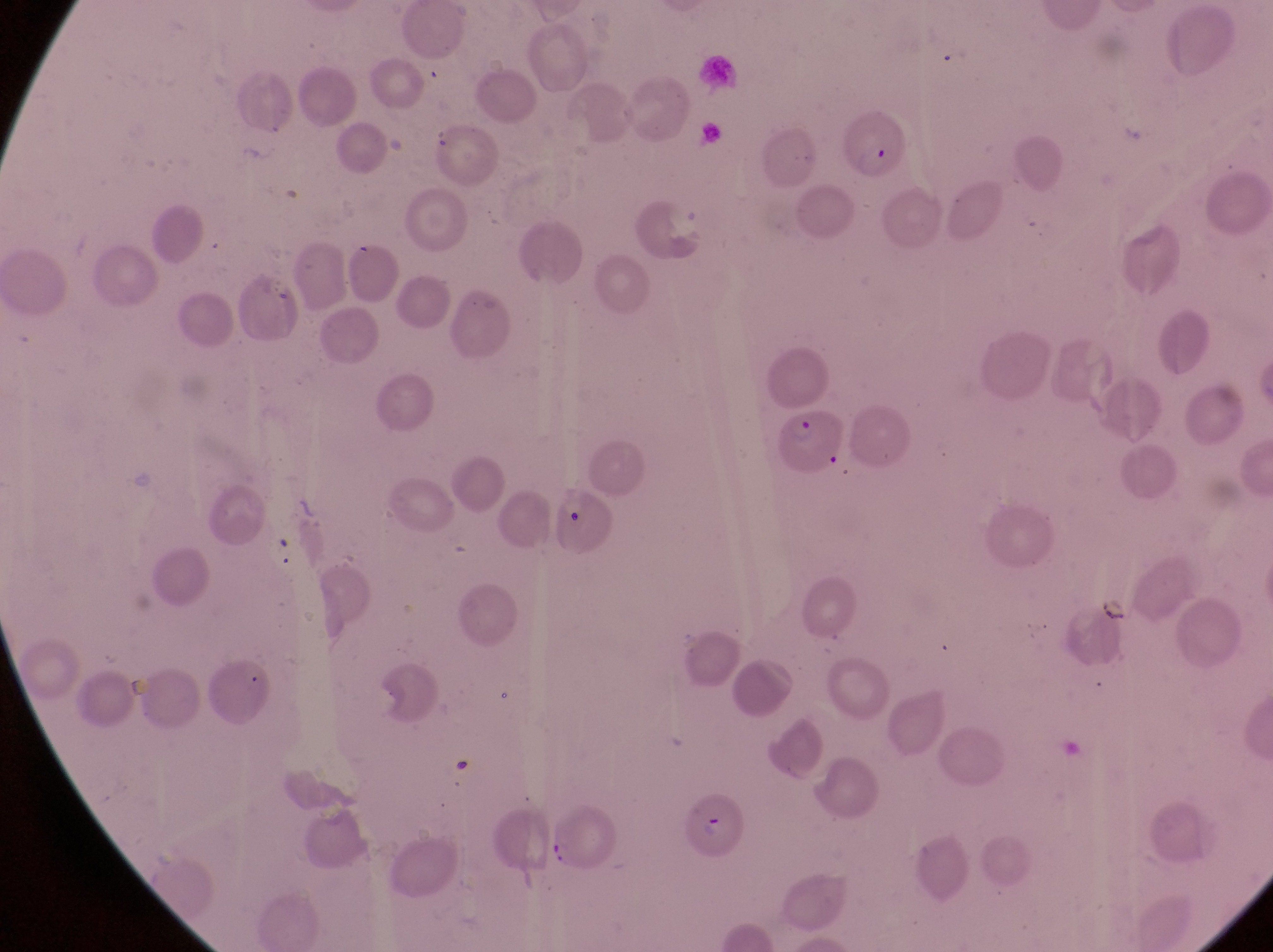
{
  "magnification": "1000x",
  "image_size": "1273×952 pixels",
  "field_of_view": "single",
  "country": "Uganda",
  "preparation": "thin blood film",
  "parasitised_red_blood_cell_locations": "approximate bounding boxes as (left, top, right, bottom) in pixels: (847, 104, 907, 182), (779, 400, 846, 478), (556, 480, 623, 562), (686, 792, 744, 862)",
  "capture": "smartphone photograph through the eyepiece of an Olympus CX-23 microscope"
}